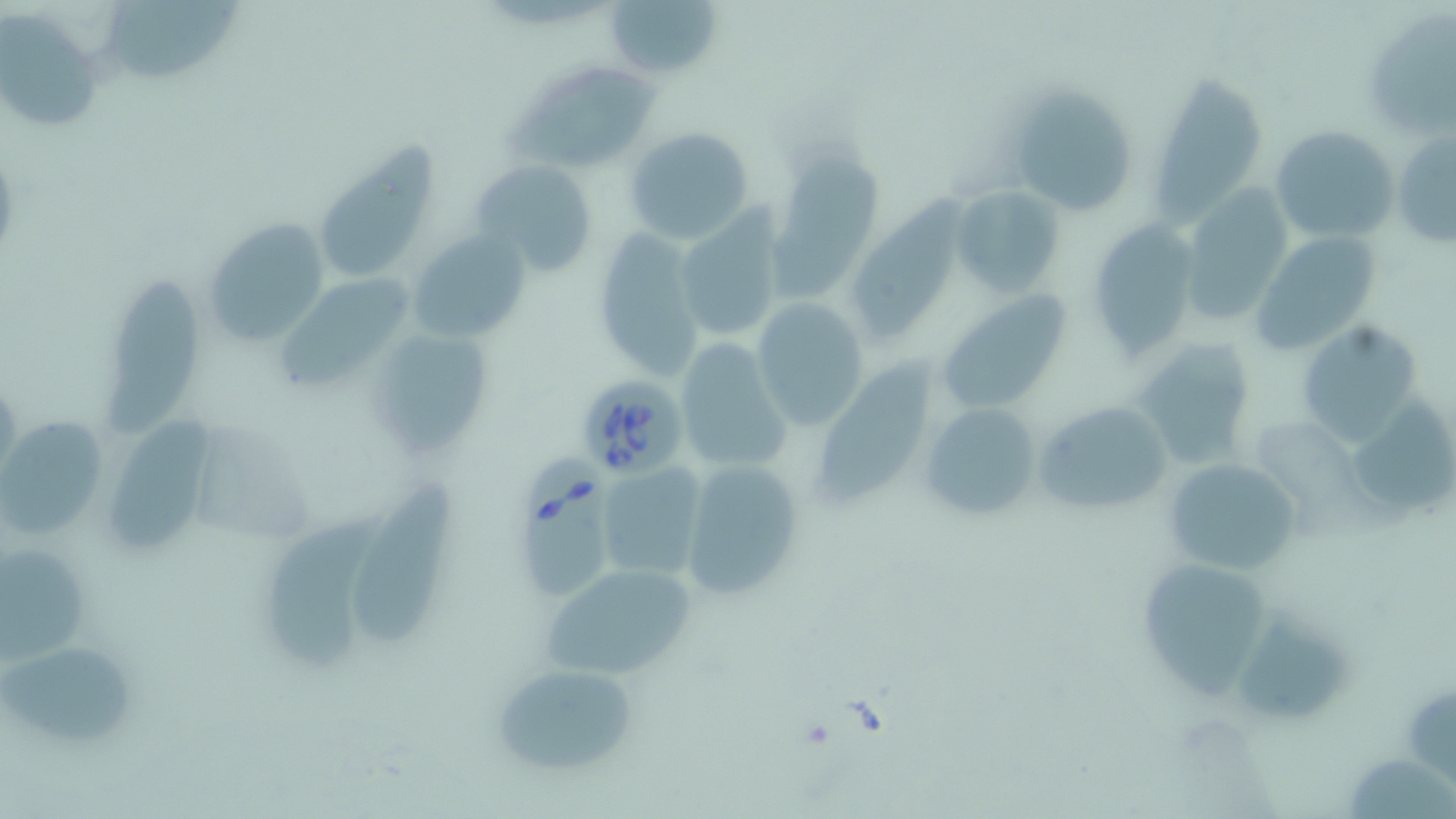
Approximate bounding boxes as (x1, y1, x2, y2) in pixels. Babesia divergens-infected red blood cell locations: (574, 374, 690, 483), (517, 450, 608, 606). Uninfected red blood cell locations: (102, 0, 246, 86), (605, 0, 726, 81), (1360, 7, 1456, 143), (0, 11, 107, 135), (488, 63, 665, 167), (1152, 67, 1270, 218), (1007, 85, 1139, 217), (1269, 125, 1399, 244), (623, 126, 755, 246), (1392, 127, 1455, 251), (316, 130, 437, 280), (771, 134, 875, 301), (470, 159, 597, 276), (852, 178, 970, 342), (953, 183, 1065, 299), (1179, 183, 1295, 322), (671, 206, 788, 342), (203, 214, 329, 349), (1086, 222, 1200, 360), (406, 231, 529, 344), (590, 231, 704, 379), (1248, 231, 1385, 354), (279, 265, 421, 392), (101, 270, 202, 443), (939, 292, 1070, 414), (752, 298, 869, 429), (1297, 319, 1425, 447), (363, 324, 494, 462), (675, 337, 793, 475), (1131, 339, 1255, 470), (824, 342, 940, 514), (1353, 393, 1453, 512), (1035, 399, 1175, 519), (918, 400, 1041, 523), (99, 413, 217, 558), (1, 418, 110, 539), (1257, 422, 1377, 537), (1161, 457, 1299, 576), (678, 458, 808, 603), (595, 464, 708, 585), (351, 478, 465, 649), (265, 496, 397, 671), (0, 538, 97, 670), (1134, 553, 1279, 701), (540, 560, 699, 682), (1240, 602, 1355, 729), (4, 636, 136, 750), (487, 660, 639, 775), (1349, 749, 1456, 818). Slide-level diagnosis: Babesia divergens. Thin blood smear. Image is 1456×819 pixels. May-Grünwald-Giemsa stain. Light microscopy. Captured at 1000x magnification. One field of a larger specimen.